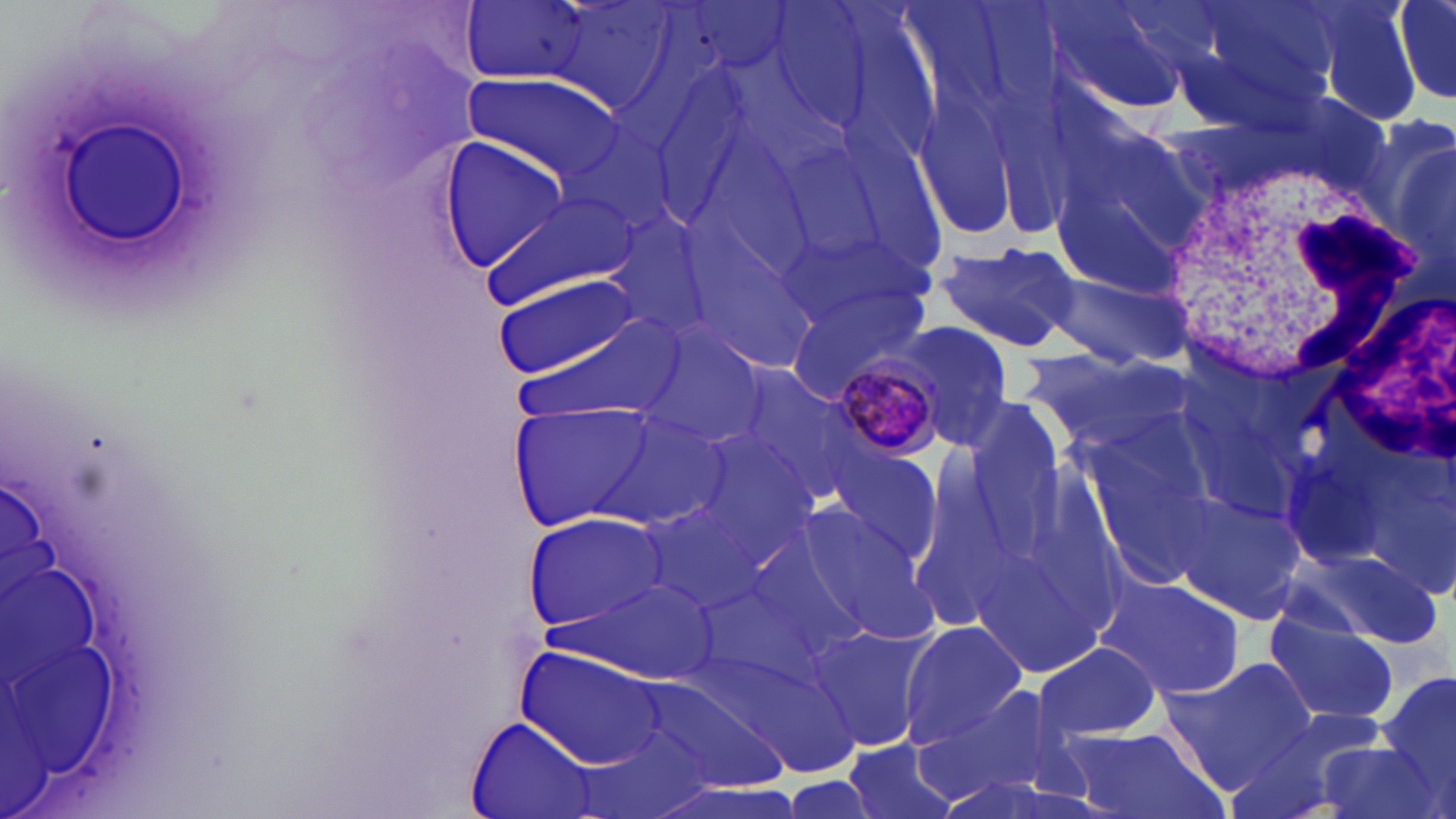

Summary:
  - Coordinate format: approximate bounding boxes as named x1/y1/x2/y2 corners in pixels
  - Uninfected red blood cell locations: (x1=539, y1=0, x2=683, y2=117), (x1=1037, y1=0, x2=1196, y2=119), (x1=1158, y1=0, x2=1340, y2=133), (x1=1298, y1=0, x2=1429, y2=126), (x1=1392, y1=0, x2=1456, y2=102), (x1=457, y1=1, x2=594, y2=85), (x1=460, y1=73, x2=622, y2=181), (x1=909, y1=91, x2=1029, y2=245), (x1=769, y1=117, x2=959, y2=308), (x1=1370, y1=118, x2=1456, y2=286), (x1=435, y1=139, x2=570, y2=267), (x1=479, y1=184, x2=639, y2=314), (x1=1053, y1=185, x2=1189, y2=303), (x1=595, y1=209, x2=721, y2=344), (x1=673, y1=210, x2=827, y2=379), (x1=932, y1=240, x2=1083, y2=352), (x1=1044, y1=269, x2=1197, y2=371), (x1=494, y1=276, x2=641, y2=378), (x1=782, y1=283, x2=933, y2=405), (x1=500, y1=310, x2=689, y2=436), (x1=893, y1=317, x2=1020, y2=451), (x1=625, y1=319, x2=772, y2=455), (x1=1022, y1=345, x2=1190, y2=450), (x1=723, y1=361, x2=865, y2=502), (x1=505, y1=399, x2=661, y2=534), (x1=593, y1=407, x2=737, y2=530), (x1=826, y1=442, x2=946, y2=568), (x1=1177, y1=489, x2=1313, y2=626), (x1=637, y1=491, x2=785, y2=615), (x1=786, y1=503, x2=935, y2=643), (x1=521, y1=513, x2=667, y2=635), (x1=1287, y1=546, x2=1440, y2=650), (x1=1095, y1=572, x2=1247, y2=701), (x1=1266, y1=615, x2=1397, y2=726), (x1=807, y1=621, x2=941, y2=754), (x1=899, y1=621, x2=1026, y2=748), (x1=1034, y1=640, x2=1162, y2=742), (x1=520, y1=645, x2=669, y2=769), (x1=1170, y1=656, x2=1321, y2=783), (x1=1378, y1=668, x2=1456, y2=794), (x1=917, y1=686, x2=1081, y2=808), (x1=1222, y1=714, x2=1382, y2=819), (x1=467, y1=719, x2=601, y2=819), (x1=1058, y1=729, x2=1216, y2=819), (x1=1312, y1=737, x2=1447, y2=819), (x1=843, y1=739, x2=962, y2=819)
  - White blood cell locations: (x1=1157, y1=158, x2=1424, y2=400)
  - Plasmodium malariae-infected red blood cell locations: (x1=823, y1=345, x2=955, y2=464)
  - Slide-level diagnosis: Plasmodium malariae
  - Preparation: thin blood film
  - Magnification: 1000x
  - Image size: 1456×819 pixels
  - Modality: light microscopy
  - Field of view: one of a larger specimen
  - Stain: May-Grünwald-Giemsa